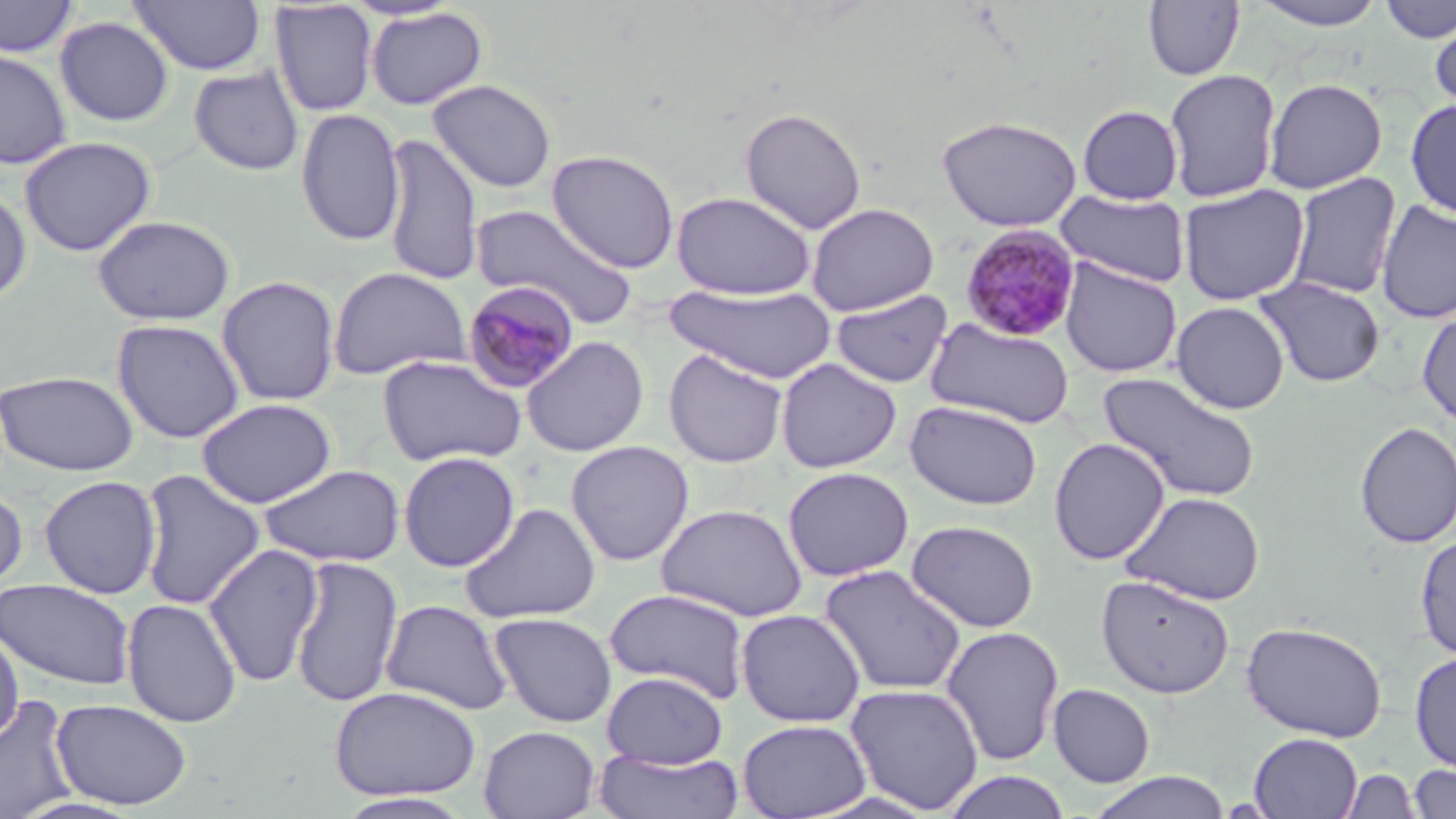

Summary:
  - Coordinate format: approximate bounding boxes as (x1, y1, x2, y2) in pixels
  - Plasmodium malariae-infected red blood cell locations: (959, 225, 1082, 342), (462, 280, 580, 395)
  - Uninfected red blood cell locations: (0, 0, 80, 59), (128, 0, 266, 76), (1248, 0, 1387, 30), (1380, 0, 1455, 43), (1144, 1, 1245, 81), (269, 2, 379, 117), (366, 7, 489, 110), (1429, 15, 1456, 116), (54, 16, 174, 127), (0, 47, 72, 169), (189, 66, 304, 176), (1163, 68, 1282, 203), (1264, 77, 1387, 194), (427, 78, 557, 193), (1405, 98, 1456, 218), (1077, 104, 1183, 206), (739, 107, 867, 234), (295, 108, 405, 247), (936, 114, 1083, 232), (381, 133, 483, 287), (19, 136, 157, 257), (546, 149, 680, 273), (1286, 172, 1401, 300), (0, 183, 32, 304), (1178, 184, 1309, 306), (671, 190, 817, 300), (1056, 190, 1191, 288), (1375, 199, 1456, 324), (806, 202, 939, 316), (470, 204, 640, 328), (91, 215, 235, 325), (1059, 259, 1182, 378), (327, 266, 472, 380), (215, 275, 341, 406), (1254, 276, 1386, 387), (665, 283, 838, 384), (831, 290, 953, 389), (1171, 301, 1289, 414), (1417, 310, 1456, 428), (926, 317, 1075, 429), (111, 318, 245, 444), (521, 335, 649, 457), (663, 348, 788, 468), (377, 355, 526, 468), (775, 358, 902, 474), (0, 370, 139, 476), (1099, 372, 1261, 503), (196, 398, 336, 508), (905, 400, 1043, 511), (1354, 422, 1456, 548), (1048, 436, 1170, 566), (565, 440, 694, 567), (397, 451, 521, 572), (257, 463, 406, 567), (782, 466, 914, 582), (137, 469, 266, 611), (39, 475, 162, 599), (0, 486, 29, 599), (1122, 491, 1266, 605), (655, 502, 808, 622), (459, 503, 601, 624), (906, 519, 1039, 632), (1415, 533, 1456, 661), (203, 543, 325, 688), (289, 556, 402, 709), (818, 564, 968, 696), (1096, 574, 1236, 699), (0, 577, 134, 691), (603, 586, 751, 703), (121, 597, 243, 727), (380, 599, 514, 715), (736, 608, 867, 727), (489, 611, 617, 728), (1241, 620, 1387, 743), (0, 626, 23, 746), (940, 626, 1065, 766), (1409, 651, 1456, 772), (602, 670, 727, 769), (844, 683, 985, 815), (1048, 684, 1155, 787), (329, 685, 482, 801), (0, 694, 80, 819), (52, 699, 192, 810), (737, 718, 871, 819), (478, 725, 600, 819), (1248, 732, 1362, 818), (593, 749, 744, 819), (1407, 763, 1456, 819), (1340, 769, 1422, 818), (941, 771, 1074, 819), (1088, 771, 1232, 819), (334, 792, 475, 818)
  - Slide-level diagnosis: Plasmodium malariae
  - Image size: 1456×819 pixels
  - Modality: optical microscopy
  - Stain: May-Grünwald-Giemsa
  - Field of view: one of a larger specimen
  - Preparation: thin blood film
  - Magnification: 1000x